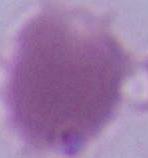

Summary:
  - Identification: red blood cell
  - Magnification: 1000x
  - Modality: photomicrograph